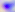 Toxoplasma gondii is seen. 400x magnification. Photomicrograph.